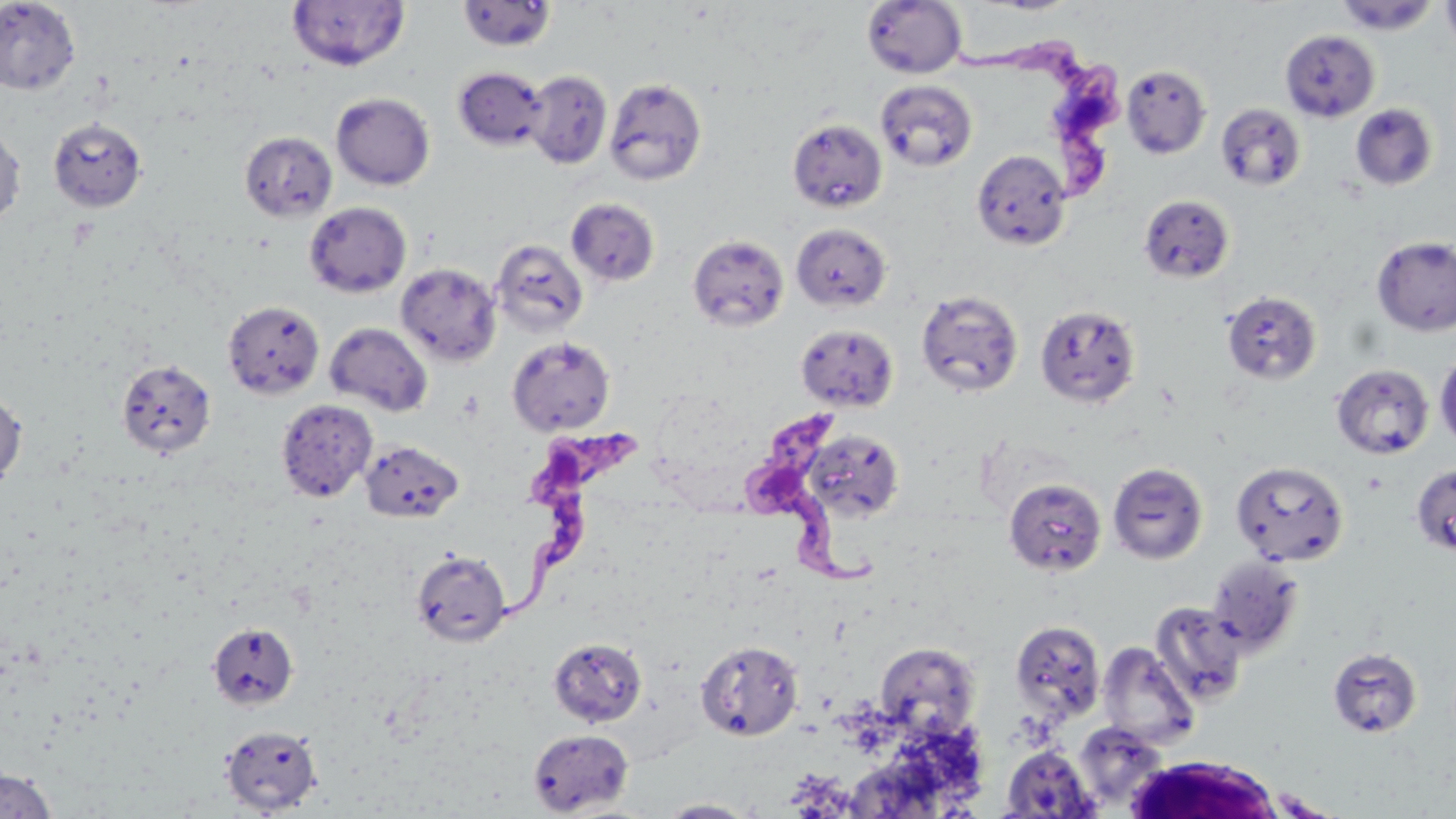
Summary:
  - Coordinate format: approximate bounding boxes as [x1, y1, x2, y2] in pixels
  - Trypanosoma brucei locations: [952, 38, 1129, 198], [741, 413, 892, 588], [499, 419, 653, 620]
  - Uninfected red blood cell locations: [287, 0, 410, 72], [1335, 0, 1440, 34], [1440, 0, 1456, 55], [0, 1, 81, 96], [457, 1, 557, 51], [862, 1, 967, 78], [1280, 29, 1380, 121], [1121, 65, 1211, 158], [454, 67, 549, 151], [524, 70, 613, 168], [604, 77, 708, 185], [875, 79, 978, 172], [331, 92, 435, 190], [1216, 102, 1306, 191], [1351, 103, 1437, 191], [48, 117, 147, 212], [787, 118, 888, 213], [0, 124, 26, 231], [239, 131, 338, 223], [971, 149, 1072, 251], [1138, 194, 1234, 283], [566, 197, 660, 286], [304, 202, 411, 297], [791, 223, 891, 312], [688, 234, 789, 331], [1371, 236, 1456, 336], [491, 239, 589, 336], [395, 263, 502, 366], [916, 289, 1024, 397], [1222, 290, 1322, 385], [222, 300, 325, 399], [1035, 305, 1141, 407], [325, 322, 433, 416], [795, 323, 899, 412], [507, 336, 616, 436], [1434, 352, 1456, 450], [117, 359, 216, 458], [1331, 364, 1434, 459], [0, 388, 27, 492], [275, 399, 377, 502], [803, 429, 905, 522], [360, 440, 464, 523], [1230, 460, 1349, 566], [1108, 462, 1208, 564], [1411, 463, 1456, 556], [1003, 477, 1107, 576], [410, 550, 512, 647], [1206, 555, 1305, 657], [1150, 601, 1249, 706], [1010, 619, 1107, 723], [206, 622, 299, 710], [548, 638, 647, 727], [695, 640, 804, 741], [1097, 641, 1200, 751], [875, 642, 981, 739], [1328, 647, 1422, 738], [1073, 721, 1168, 811], [220, 724, 322, 814], [528, 728, 634, 816], [1001, 745, 1099, 817], [0, 767, 56, 818], [658, 799, 759, 818]
  - White blood cell locations: [1122, 755, 1287, 818]
  - Slide-level diagnosis: Trypanosoma brucei
  - Preparation: thin blood film
  - Field of view: single
  - Stain: May-Grünwald-Giemsa
  - Magnification: 1000x
  - Image size: 1456×819 pixels
  - Modality: optical microscopy